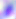
{
  "magnification": "400x",
  "modality": "photomicrograph",
  "identification": "Toxoplasma gondii"
}